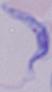
Summary:
  - Identification: trypanosome
  - Modality: photomicrograph
  - Magnification: 1000x